Comment on the morphology of the red blood cells.
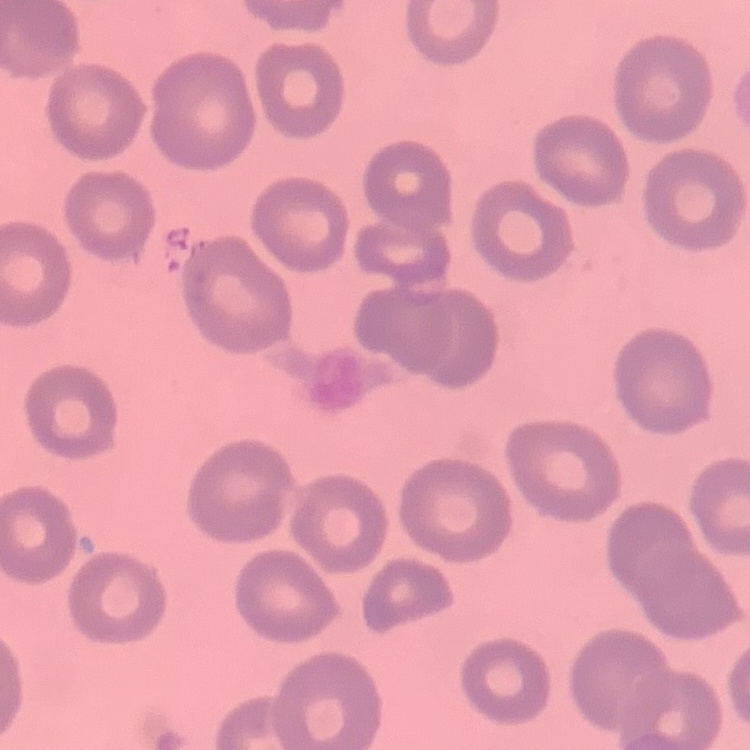
They show no rouleaux formation.

Thin blood film. One tile cut from a larger photomicrograph. Stained with either Field's or Giemsa.